Classify this cell by malaria status.
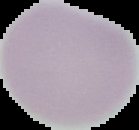
It is uninfected.

preparation = thin blood film
image size = 139×130 pixels
image type = segmented cell region on a black background